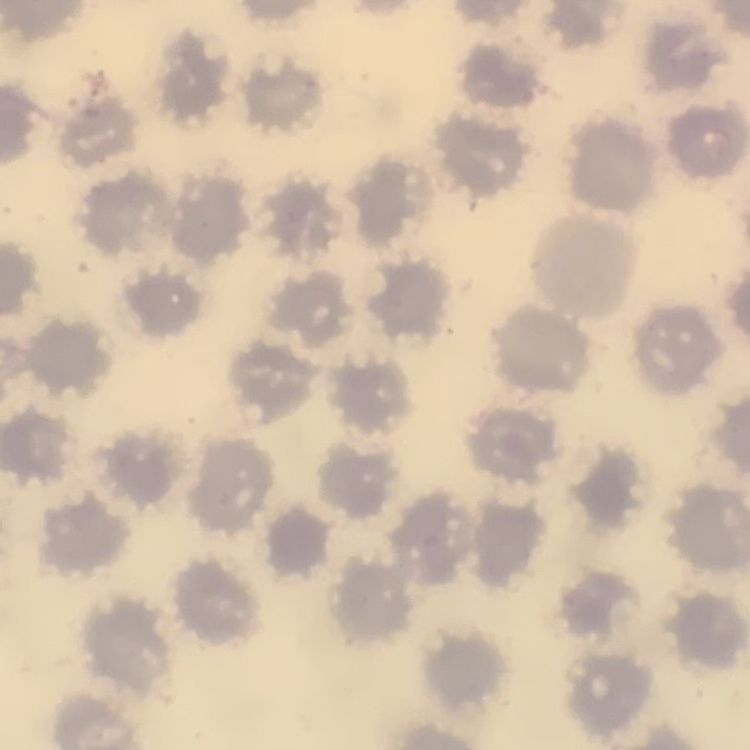
The red blood cells show no rouleaux formation. Thin blood film. Square crop of a larger photomicrograph. Field's or Giemsa stain.